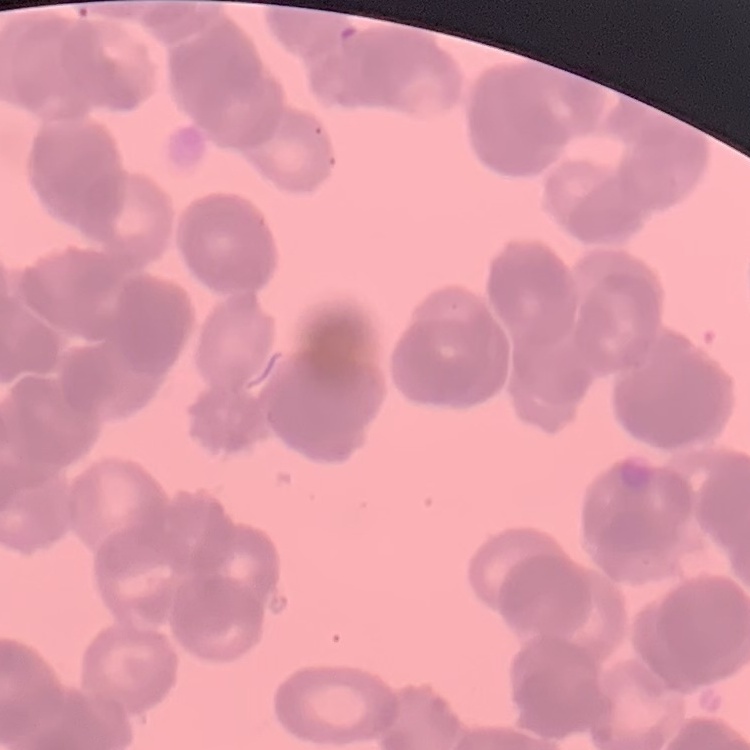
The erythrocytes exhibit rouleaux formation. Stained with either Field's or Giemsa. Thin blood smear. Square crop of a larger photomicrograph.